Name the blood parasite species.
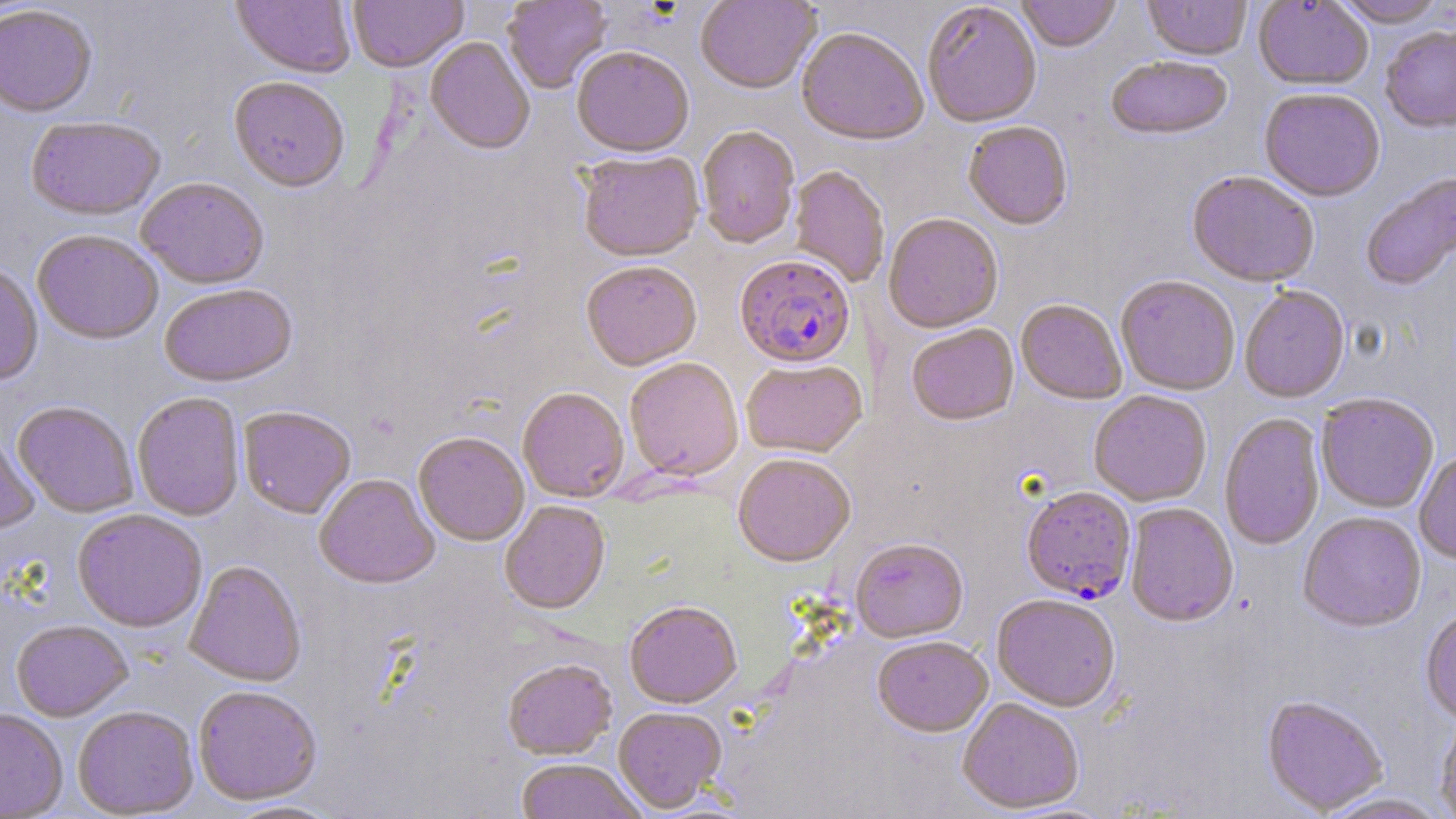

Plasmodium falciparum.

uninfected_red_blood_cell_locations: 'approximate bounding boxes as [x1, y1, x2, y2] in pixels: [231, 0, 356, 81], [348, 0, 468, 75], [502, 0, 612, 95], [1017, 0, 1122, 54], [1142, 0, 1251, 63], [1332, 0, 1449, 30], [694, 1, 821, 96], [1254, 1, 1373, 92], [923, 4, 1041, 131], [0, 7, 97, 120], [1380, 28, 1456, 135], [796, 30, 928, 149], [425, 38, 535, 157], [571, 48, 694, 161], [1106, 58, 1232, 143], [228, 79, 350, 196], [1259, 90, 1385, 204], [25, 118, 165, 224], [962, 123, 1073, 232], [697, 127, 800, 251], [577, 153, 704, 265], [789, 167, 889, 288], [1187, 173, 1319, 290], [1361, 173, 1456, 293], [136, 179, 268, 291], [883, 215, 1003, 335], [32, 232, 163, 346], [581, 264, 702, 373], [0, 265, 43, 387], [1116, 278, 1239, 397], [159, 286, 298, 390], [1240, 288, 1350, 404], [1016, 301, 1126, 406], [906, 326, 1019, 428], [625, 360, 743, 483], [741, 361, 867, 459], [518, 388, 629, 504], [1089, 392, 1211, 507], [132, 394, 245, 522], [1316, 395, 1438, 514], [13, 402, 138, 518], [238, 407, 356, 521], [1220, 414, 1325, 552], [0, 431, 40, 535], [413, 435, 529, 547], [1416, 451, 1456, 564], [733, 456, 855, 569], [314, 475, 439, 591], [499, 502, 611, 617], [1124, 505, 1239, 629], [72, 510, 208, 634], [1298, 513, 1427, 635], [850, 541, 969, 645], [184, 562, 307, 687], [992, 596, 1119, 714], [625, 603, 742, 710], [1420, 610, 1456, 726], [11, 621, 133, 722], [873, 638, 993, 739], [502, 660, 617, 762], [193, 687, 323, 806], [1262, 697, 1387, 815], [958, 700, 1084, 814], [73, 706, 199, 818], [613, 708, 727, 814], [0, 709, 68, 818], [1435, 714, 1456, 819], [513, 761, 647, 819], [1315, 793, 1451, 819]'
modality: light microscopy
field_of_view: single
preparation: thin blood smear
stain: May-Grünwald-Giemsa
image_size: 1456×819 pixels
magnification: 1000x
plasmodium_falciparum_infected_red_blood_cell_locations: 'approximate bounding boxes as [x1, y1, x2, y2] in pixels: [735, 257, 855, 371], [1021, 488, 1136, 605]'